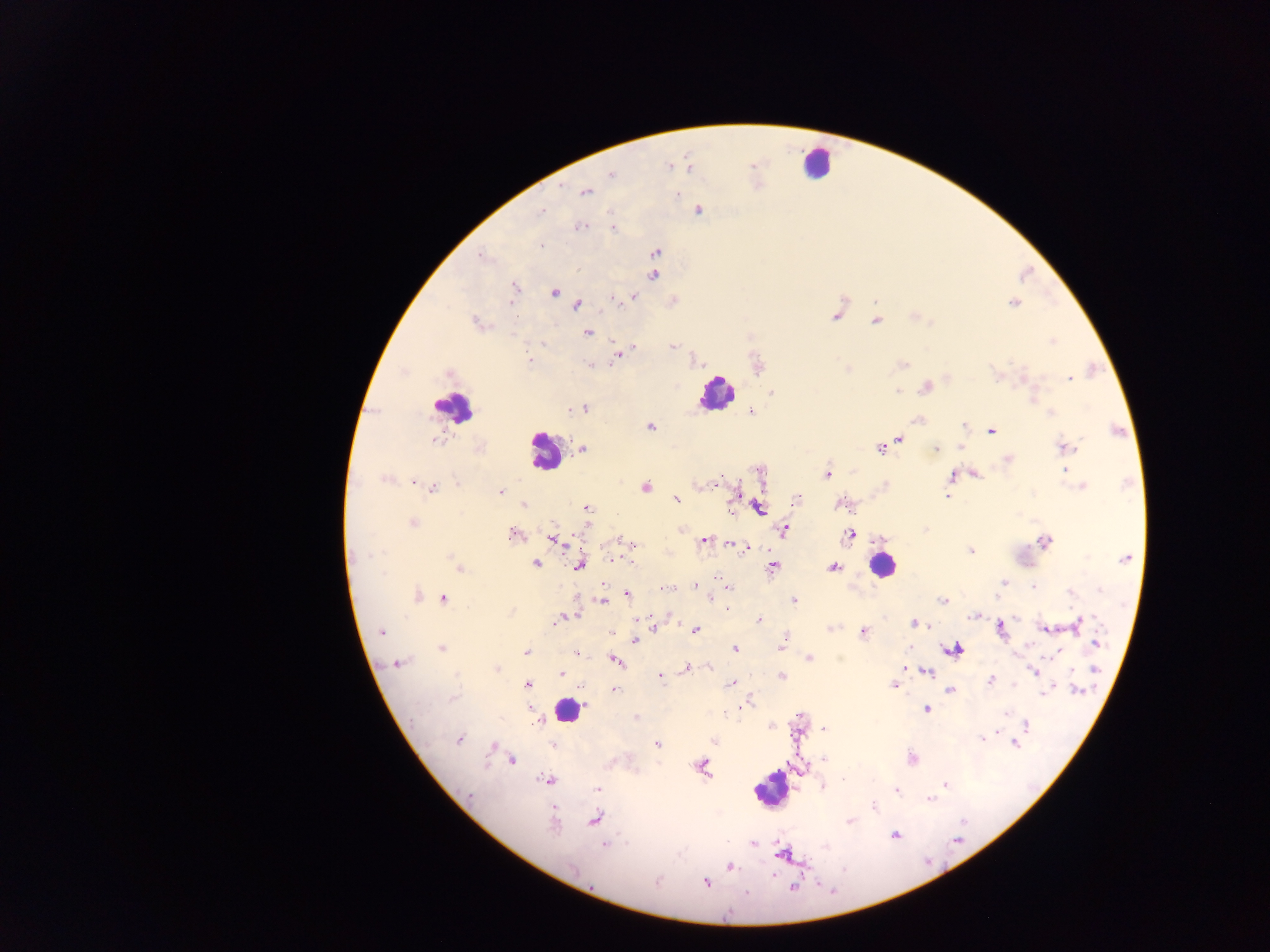

{
  "field_of_view": "single",
  "plasmodium_parasite_locations": "approximate centers as (x, y) in pixels: (669, 166), (688, 167), (611, 174), (585, 192), (677, 194), (698, 209), (540, 211), (578, 226), (614, 227), (541, 247), (655, 252), (482, 255), (654, 267), (654, 275), (514, 287), (553, 292), (632, 296), (613, 298), (1013, 303), (576, 305), (836, 313), (914, 317), (876, 320), (476, 323), (588, 332), (1052, 341), (543, 342), (671, 344), (619, 352), (528, 359), (901, 363), (591, 365), (758, 366), (449, 372), (998, 375), (1069, 377), (925, 386), (897, 391), (771, 392), (1033, 395), (571, 407), (581, 407), (750, 410), (1051, 412), (917, 420), (649, 426), (964, 426), (990, 430), (434, 439), (900, 439), (881, 447), (962, 447), (1064, 447), (582, 449), (934, 449), (1007, 459), (759, 470), (1066, 472), (826, 473), (973, 473), (967, 474), (952, 476), (385, 479), (414, 481), (457, 484), (1082, 486), (432, 487), (644, 487), (501, 491), (948, 495), (677, 499), (796, 499), (523, 504), (842, 505), (757, 507), (586, 509), (412, 522), (783, 530), (514, 533), (849, 535), (553, 539), (704, 539), (1044, 541), (729, 543), (631, 544), (746, 547), (970, 550), (1124, 558), (630, 561), (535, 564), (579, 564), (458, 566), (773, 567), (832, 567), (717, 577), (1003, 582), (695, 584), (1034, 585), (665, 588), (728, 589), (626, 593), (416, 595), (442, 597), (710, 598), (602, 600), (794, 600), (943, 600), (727, 606), (973, 614), (570, 615), (563, 617), (671, 618), (759, 621), (1078, 622), (915, 624), (653, 628), (829, 628), (1000, 628), (1045, 628), (694, 630), (862, 631), (382, 632), (612, 632), (634, 639), (783, 639), (782, 643), (1095, 644), (441, 648), (735, 648), (952, 648), (527, 652), (575, 652), (809, 657), (615, 660), (396, 664), (709, 666), (686, 668), (495, 669), (902, 669), (927, 671), (1033, 671), (1072, 672), (560, 674), (660, 676), (781, 677), (990, 680), (730, 683), (527, 684), (894, 684), (614, 689), (950, 689), (1047, 689), (1043, 692), (745, 701), (925, 709), (798, 716), (636, 718), (541, 720), (1025, 725), (772, 726), (824, 729), (996, 733), (458, 738), (980, 739), (714, 740), (1014, 742), (656, 743), (493, 746), (910, 757), (510, 760), (701, 766), (549, 780), (945, 785), (823, 786), (597, 788), (895, 790), (929, 800), (873, 807), (594, 819), (850, 820), (894, 835), (753, 842), (604, 844), (782, 853), (729, 866), (705, 882)",
  "capture": "mobile-phone photograph through a microscope",
  "country": "Ghana",
  "leukocyte_locations": "approximate centers as (x, y) in pixels: (815, 163), (717, 392), (453, 406), (545, 451), (883, 565), (569, 710), (771, 788)",
  "image_size": "1270×952 pixels",
  "preparation": "thick blood smear"
}